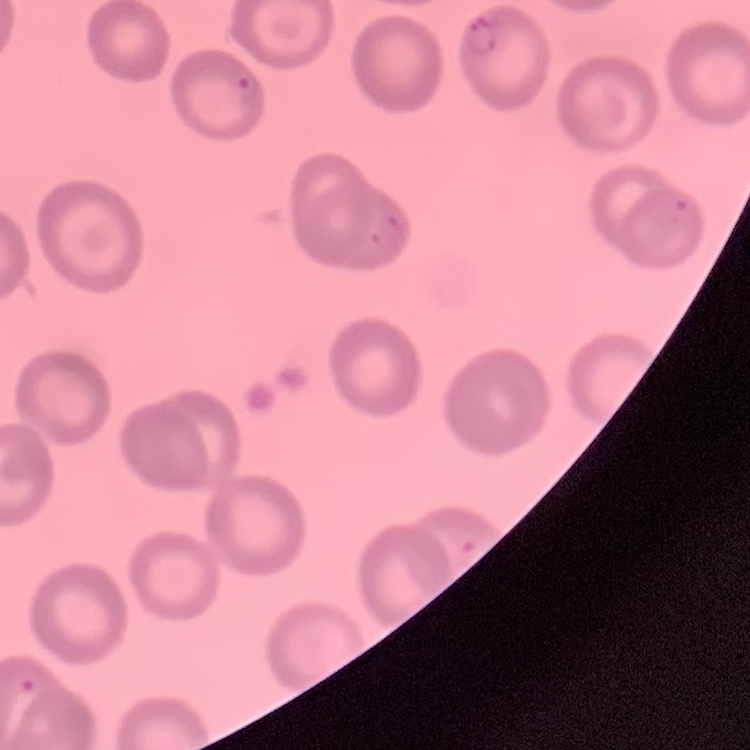

erythrocyte morphology = no rouleaux formation
preparation = thin peripheral smear
stain = Field's or Giemsa
image type = square crop of a larger photomicrograph